Report the malaria status.
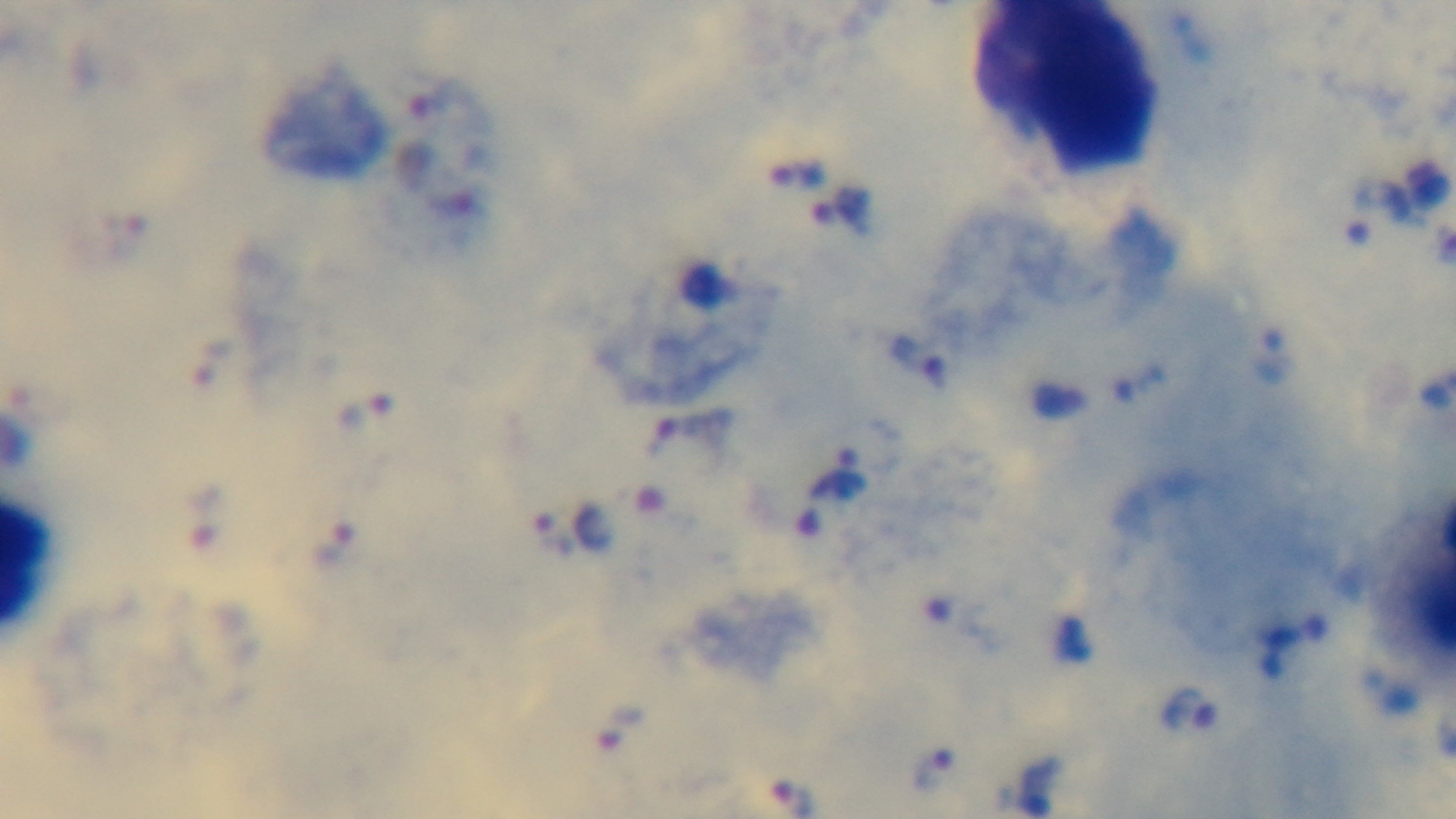
Positive.

modality: light microscopy
field_of_view: single
stain: Giemsa
capture: mounted 4K digital camera
objective: 100x oil immersion
preparation: thick smear